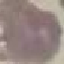
malaria_status: uninfected
stain: Giemsa
preparation: thin blood film
capture: smartphone camera at the microscope eyepiece
image_type: cell patch, automatically extracted from a larger field of view and resized to 64 × 64 pixels